Classify this cell by malaria status.
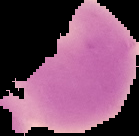

Uninfected.

{
  "image_type": "segmented cell region with the area outside set to black",
  "image_size": "139×136 pixels",
  "preparation": "thin blood smear"
}